State which parasite is depicted.
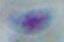

Toxoplasma gondii.

Summary:
  - Magnification: 1000x
  - Modality: micrograph